Assess the morphology of the red blood cells.
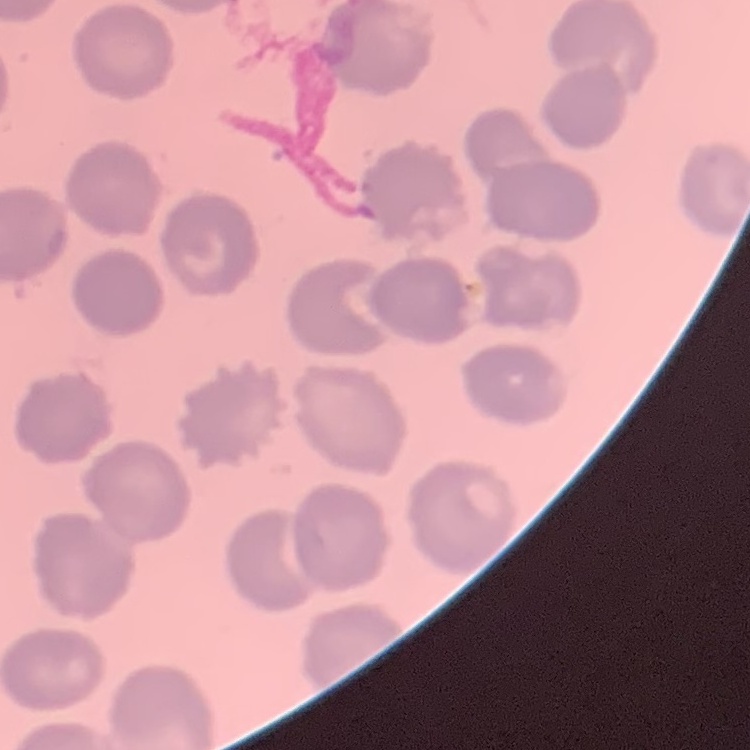
No rouleaux formation.

Thin blood film. Field's or Giemsa stain. One tile cut from a larger photomicrograph.